Describe the morphology of the erythrocytes.
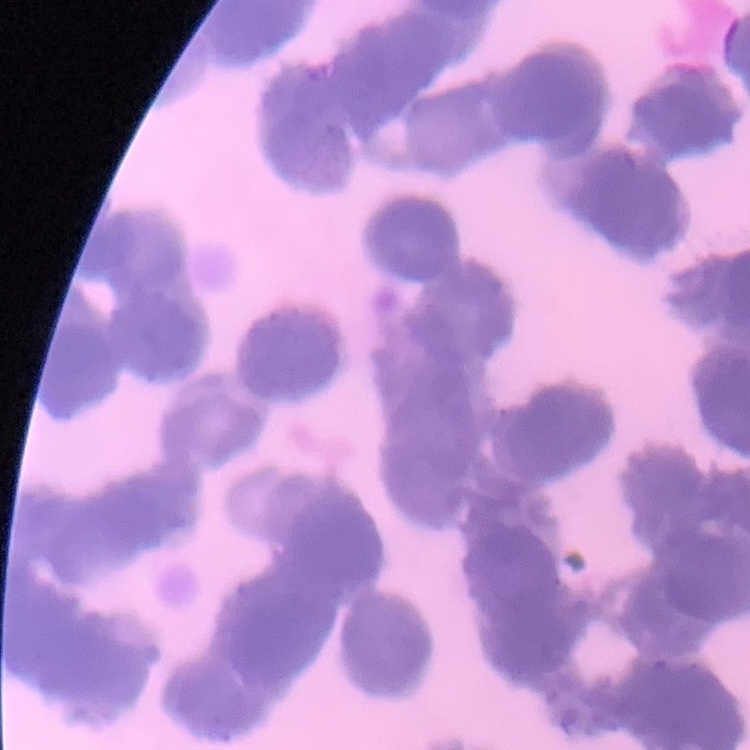

Rouleaux formation.

image_type: square crop of a larger photomicrograph
stain: Field's or Giemsa
preparation: thin blood film